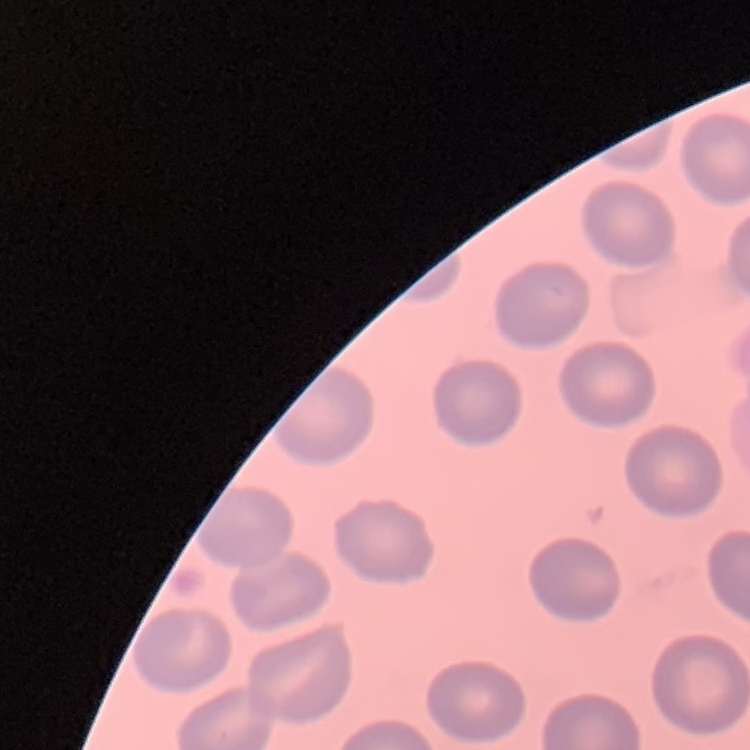

The erythrocytes exhibit no rouleaux formation. Field's or Giemsa stain. One tile cut from a larger photomicrograph. Thin blood film.